Locate every leukocyte (white blood cell).
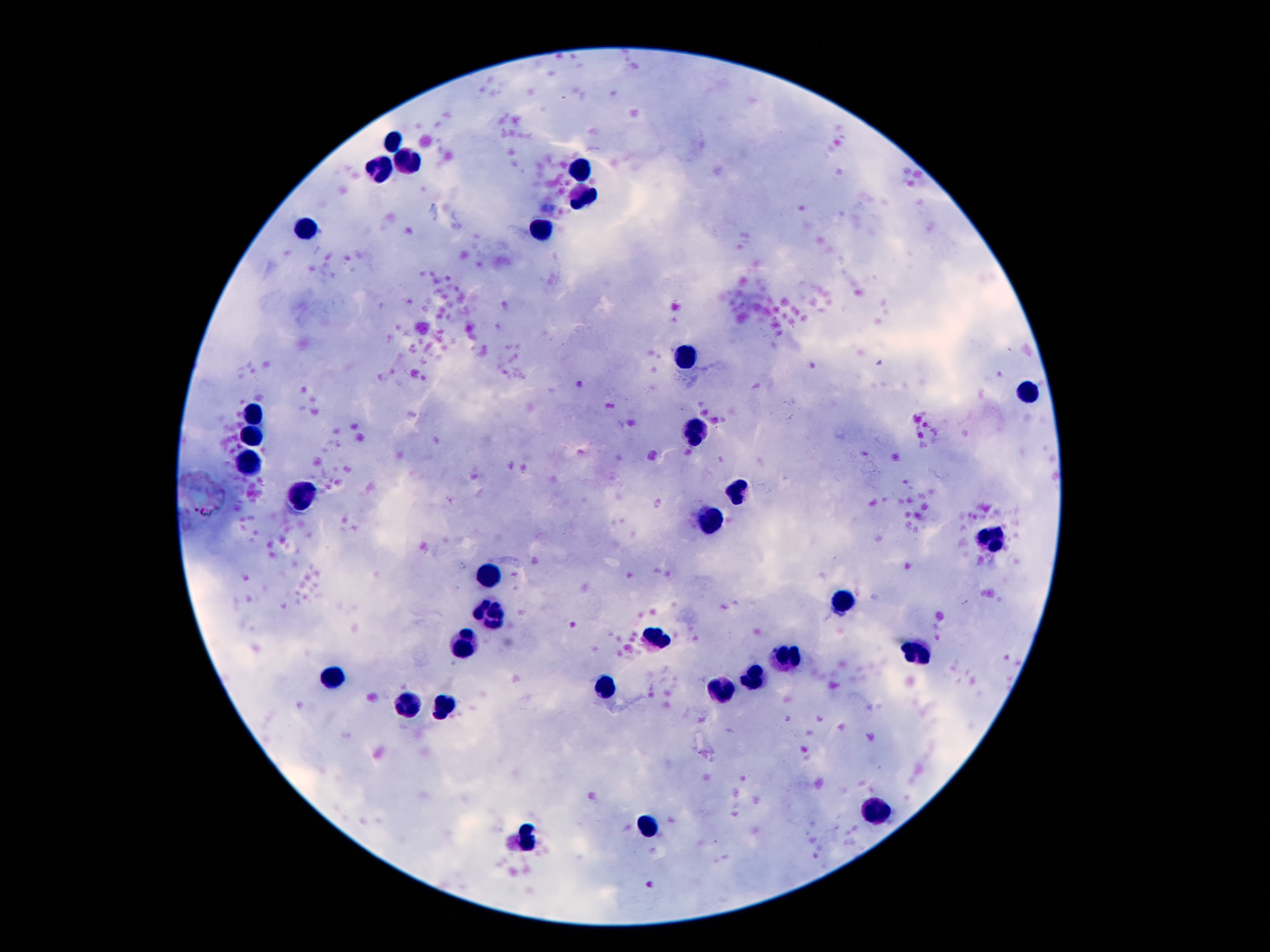

Approximate centers as [x, y] in pixels.
Leukocytes: [393, 139], [408, 162], [377, 169], [580, 171], [584, 199], [305, 229], [543, 230], [687, 355], [1028, 391], [253, 415], [696, 432], [254, 435], [251, 463], [739, 490], [305, 496], [711, 521], [993, 540], [487, 580], [841, 601], [489, 614], [657, 637], [461, 644], [914, 654], [788, 657], [331, 676], [757, 681], [606, 684], [724, 689], [408, 707], [443, 709], [872, 812], [647, 826], [528, 839].

Summary:
  - Field of view: single
  - Preparation: thick peripheral-blood smear
  - Patient malaria status: not infected
  - Stain: Giemsa
  - Image size: 1270×952 pixels
  - Magnification: 100x
  - Capture: smartphone camera through the microscope eyepiece